Assess this cell for malaria.
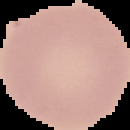
Uninfected.

preparation = thin blood smear
image type = cell region segmented out of the field of view; surrounding area masked to black
image size = 130×130 pixels